State which parasite is depicted.
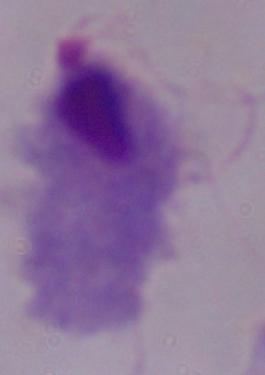

A trichomonad.

1000x magnification. Micrograph.